Identify the parasite.
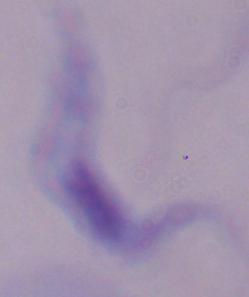

This is a trypanosome.

Captured at 1000x magnification. Micrograph.